Locate every Plasmodium parasite.
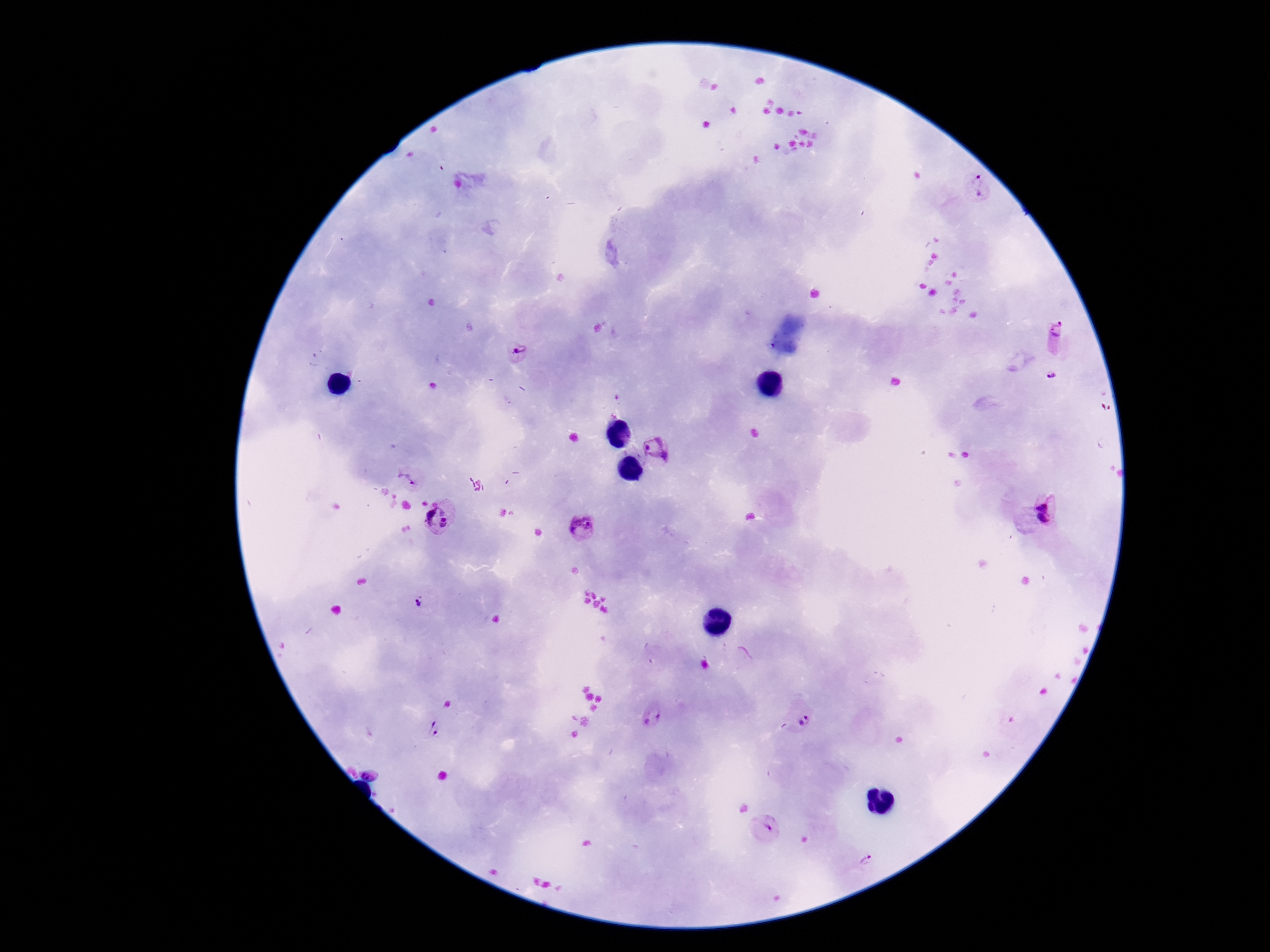
Approximate centers as [x, y] in pixels.
Plasmodium parasites: [979, 187], [1056, 335], [518, 353], [1053, 375], [657, 449], [408, 479], [1054, 510], [447, 519], [581, 527], [418, 603], [800, 715], [654, 716], [434, 729], [371, 773], [766, 827], [867, 858].

Thick peripheral-blood smear. Image is 1270×952 pixels. Patient malaria status: positive. 100x magnification. One field from this slide. Photographed through the microscope eyepiece with a smartphone camera. Giemsa stain.